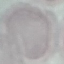
Malaria status: uninfected. Thin blood smear. Giemsa-stained preparation. Acquired by smartphone through the microscope eyepiece. Automatically extracted cell patch, resized to 64 × 64 pixels.